Locate and identify every blood parasite.
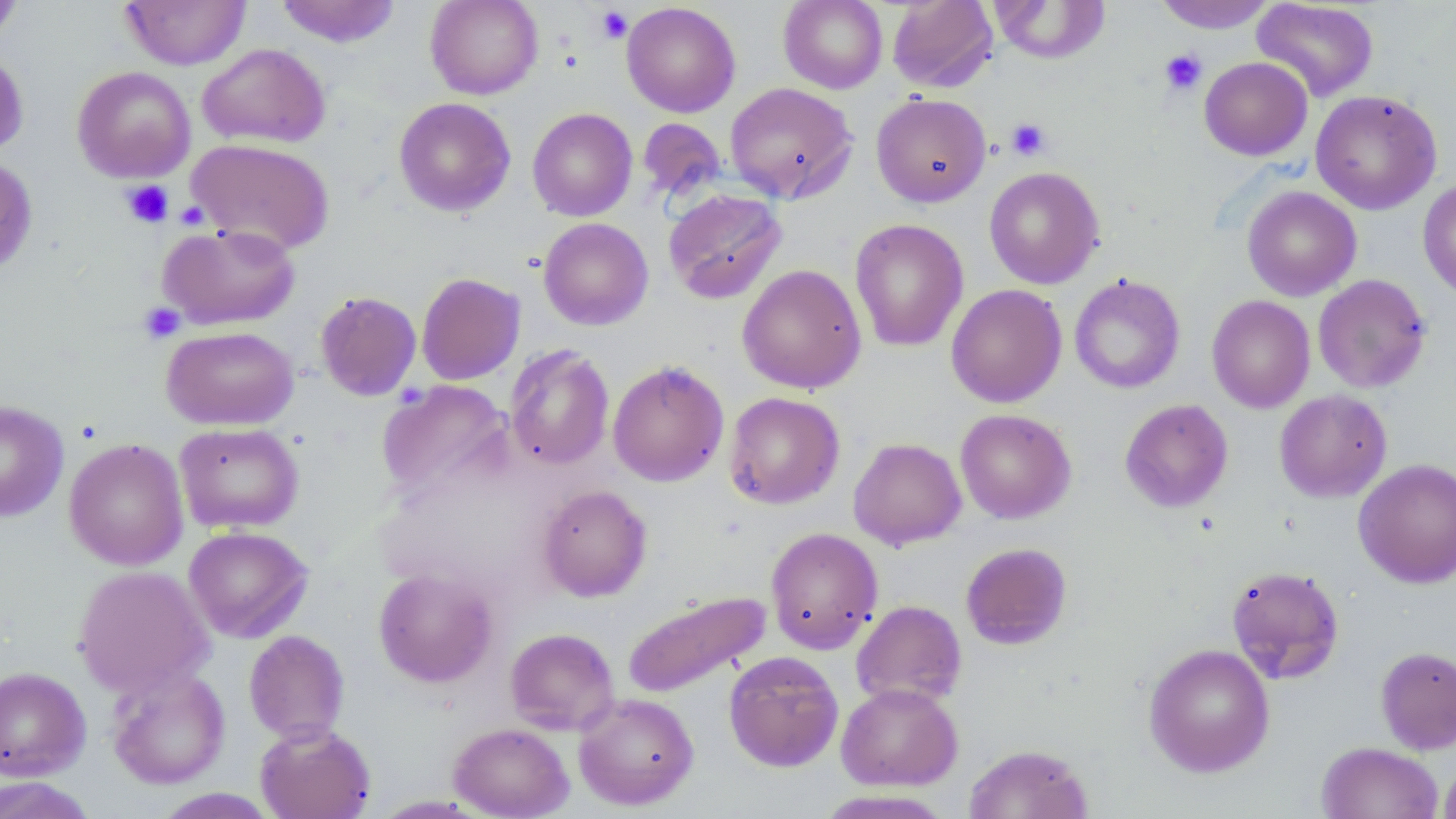

No blood parasites observed.

slide-level diagnosis = negative for blood parasites
image size = 1456×819 pixels
field of view = one of a larger specimen
uninfected red blood cell locations = approximate bounding boxes as (x1,y1)-(x2,y2) corner pairs in pixels: (121,0)-(249,69), (276,0)-(401,47), (426,0)-(543,99), (778,0)-(888,93), (888,0)-(997,93), (1153,0)-(1276,34), (1251,0)-(1379,102), (0,1)-(23,43), (991,1)-(1110,63), (621,2)-(741,118), (198,43)-(330,148), (0,49)-(29,157), (1199,56)-(1313,161), (72,66)-(196,182), (725,82)-(857,203), (1310,90)-(1442,215), (871,92)-(991,207), (393,97)-(516,216), (527,108)-(638,221), (637,118)-(727,203), (186,138)-(336,254), (0,156)-(38,276), (983,166)-(1105,289), (1418,179)-(1456,300), (1242,186)-(1362,301), (663,188)-(786,304), (538,217)-(654,330), (850,218)-(969,352), (159,222)-(301,330), (737,264)-(866,394), (416,273)-(525,385), (1069,274)-(1185,394), (1313,274)-(1431,393), (946,284)-(1068,408), (315,291)-(422,401), (1206,295)-(1315,413), (161,326)-(299,431), (504,344)-(615,471), (607,359)-(729,487), (377,380)-(513,503), (1274,389)-(1392,503), (724,392)-(844,509), (1119,398)-(1233,513), (0,401)-(69,522), (955,408)-(1076,524), (175,422)-(304,533), (848,437)-(966,549), (64,438)-(188,570), (1353,458)-(1456,588), (537,484)-(652,601), (183,526)-(313,643), (765,527)-(883,654), (960,542)-(1073,650), (1226,564)-(1345,684), (73,565)-(213,698), (373,567)-(498,688), (623,590)-(770,698), (851,600)-(967,709), (505,627)-(620,735), (243,630)-(349,744), (1143,643)-(1275,777), (1376,646)-(1456,754), (723,651)-(844,771), (0,666)-(91,780), (106,666)-(231,789), (835,683)-(963,791), (573,692)-(699,810), (254,721)-(376,819), (449,722)-(574,819), (1316,742)-(1443,819), (963,743)-(1093,819), (1438,758)-(1456,819), (0,776)-(98,819), (153,788)-(279,818), (814,789)-(955,818)
stain = May-Grünwald-Giemsa
modality = light microscopy
magnification = 1000x
platelet locations = approximate bounding boxes as (x1,y1)-(x2,y2) corner pairs in pixels: (596,6)-(633,43), (1159,48)-(1207,96), (1006,118)-(1051,161), (120,180)-(174,229), (138,302)-(186,344)
preparation = thin blood smear